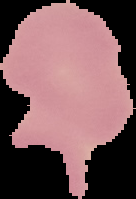

Summary:
  - Image type: segmented cell region on a black background
  - Image size: 136×199 pixels
  - Malaria status: uninfected
  - Preparation: thin blood film